Name the parasite shown.
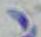

Toxoplasma gondii.

Summary:
  - Modality: micrograph
  - Magnification: 1000x